Name the cell type shown.
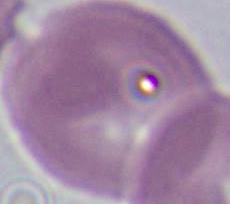

This is an erythrocyte.

modality = micrograph
magnification = 1000x